Assess for malaria.
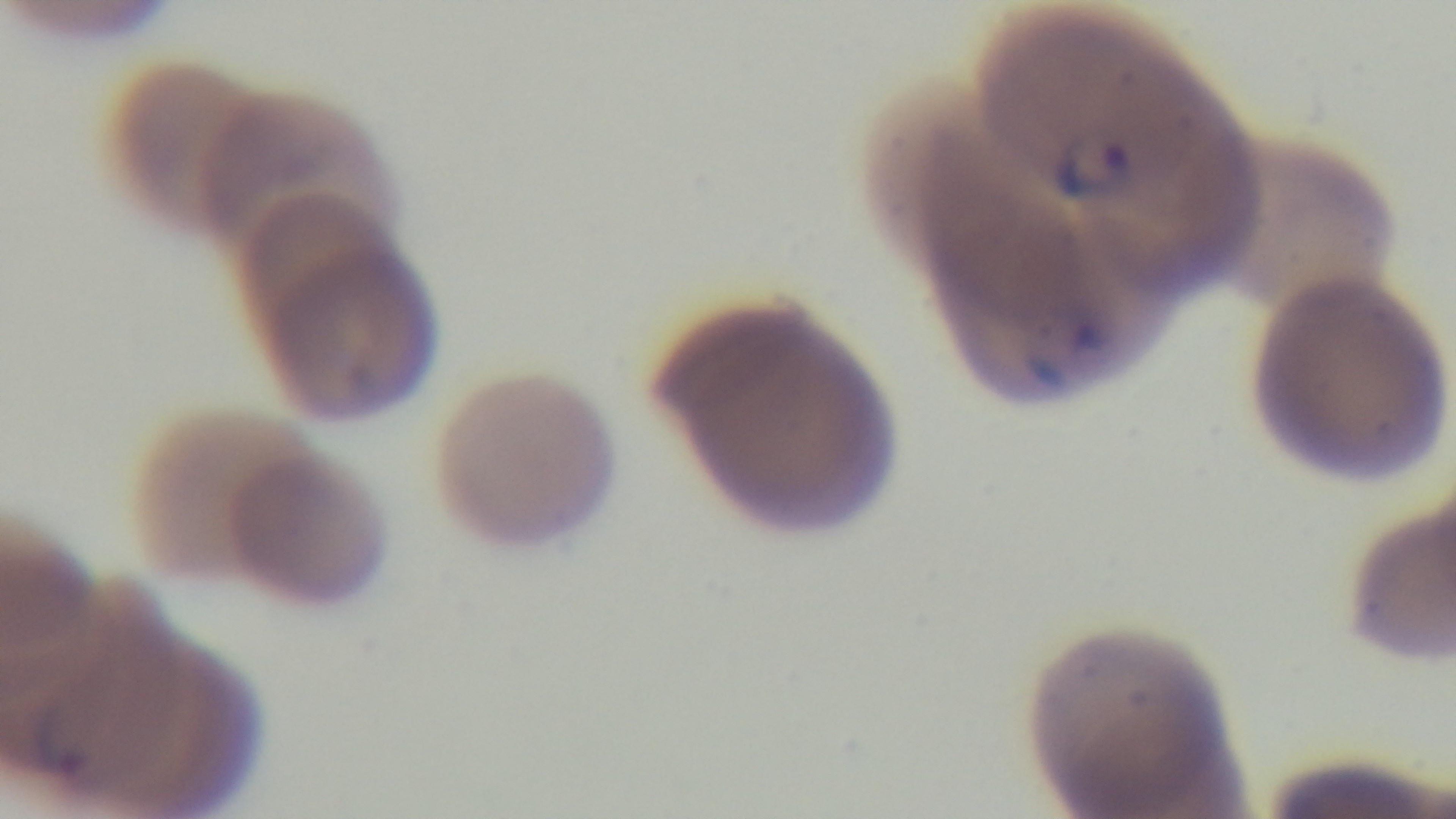

It is infected.

Summary:
  - Capture: mounted 4K digital camera
  - Stain: Giemsa
  - Objective: 100x oil immersion
  - Preparation: thin smear
  - Field of view: one from the slide
  - Modality: light microscopy